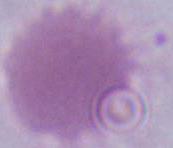
modality = photomicrograph
identification = erythrocyte
magnification = 1000x